Outline each blood parasite and name the species.
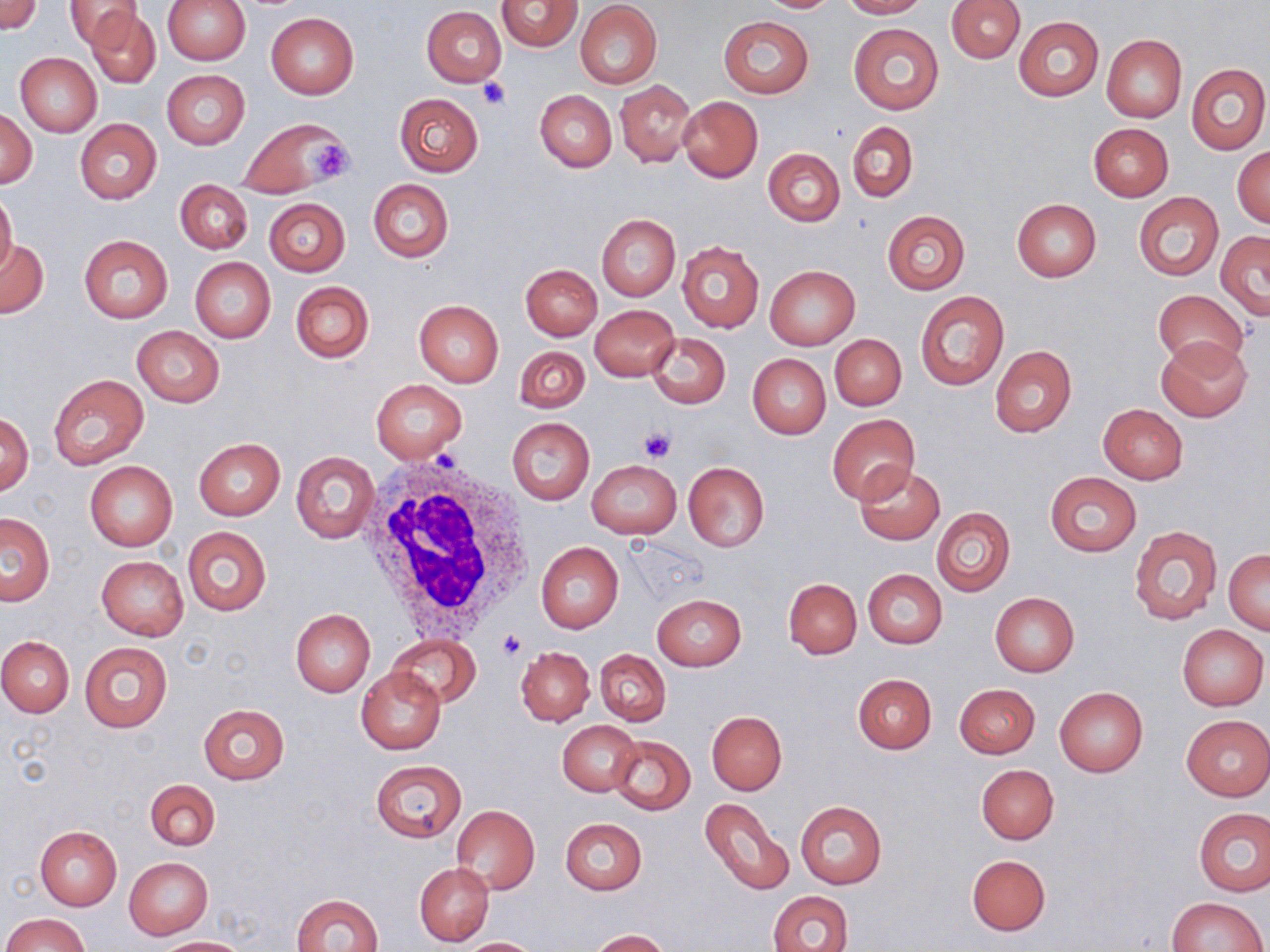

No blood parasites observed.

slide-level diagnosis = negative for blood parasites
field of view = single
image size = 1270×952 pixels
magnification = 1000x
modality = light microscopy
platelet locations = approximate bounding boxes as [x1, y1, x2, y2] in pixels: [477, 76, 511, 111], [307, 140, 355, 183], [639, 427, 674, 463], [498, 631, 525, 660]
preparation = thin blood film
uninfected red blood cell locations = approximate bounding boxes as [x1, y1, x2, y2] in pixels: [0, 0, 41, 35], [64, 0, 143, 50], [163, 0, 250, 64], [496, 0, 582, 52], [755, 0, 842, 13], [839, 0, 926, 18], [946, 0, 1025, 63], [575, 2, 663, 89], [86, 6, 161, 87], [422, 6, 506, 87], [265, 12, 360, 98], [719, 16, 813, 99], [1013, 16, 1103, 100], [848, 21, 944, 115], [1102, 35, 1186, 121], [15, 52, 102, 137], [1186, 62, 1269, 154], [162, 70, 250, 149], [615, 81, 696, 167], [535, 90, 616, 171], [394, 93, 484, 176], [678, 96, 763, 182], [2, 106, 36, 189], [237, 118, 348, 198], [75, 120, 161, 203], [847, 122, 918, 202], [1088, 123, 1173, 200], [1232, 147, 1270, 228], [763, 148, 844, 226], [367, 178, 454, 263], [175, 181, 253, 253], [0, 190, 18, 279], [1133, 192, 1223, 281], [264, 198, 350, 276], [1012, 199, 1102, 282], [882, 211, 970, 293], [597, 214, 680, 300], [1215, 230, 1270, 320], [78, 235, 173, 323], [0, 240, 48, 319], [676, 240, 764, 333], [190, 257, 276, 343], [521, 264, 601, 341], [765, 265, 860, 350], [289, 281, 375, 363], [1153, 289, 1249, 369], [914, 291, 1009, 391], [414, 300, 504, 387], [589, 305, 679, 382], [132, 325, 224, 406], [645, 331, 731, 409], [830, 334, 906, 410], [1156, 335, 1253, 423], [990, 345, 1077, 437], [514, 346, 589, 413], [748, 354, 831, 439], [48, 374, 149, 471], [370, 378, 468, 463], [1098, 403, 1189, 483], [1, 413, 34, 495], [828, 414, 919, 504], [507, 417, 595, 504], [193, 438, 285, 519], [291, 451, 380, 544], [587, 460, 681, 538], [85, 462, 177, 551], [682, 462, 770, 551], [854, 465, 944, 545], [1044, 471, 1141, 557], [931, 506, 1015, 596], [1, 512, 54, 606], [1129, 524, 1222, 624], [182, 527, 271, 615], [536, 543, 623, 634], [1225, 549, 1269, 634], [96, 555, 189, 640], [862, 568, 947, 648], [784, 578, 861, 659], [990, 592, 1080, 676], [652, 594, 746, 671], [290, 609, 375, 697], [1177, 624, 1268, 710], [386, 634, 481, 707], [0, 635, 75, 717], [80, 641, 172, 733], [516, 647, 594, 726], [595, 650, 671, 726], [357, 666, 446, 754], [852, 673, 936, 754], [954, 683, 1040, 758], [1054, 686, 1148, 777], [197, 703, 289, 784], [706, 711, 787, 794], [1181, 715, 1270, 801], [558, 720, 642, 797], [609, 735, 695, 816], [370, 760, 467, 842], [976, 764, 1059, 843], [145, 779, 221, 850], [700, 798, 793, 896], [795, 801, 888, 889], [451, 805, 540, 896], [1193, 808, 1270, 896], [559, 817, 647, 895], [34, 825, 121, 910], [967, 854, 1051, 935], [124, 857, 213, 938], [415, 862, 494, 947], [769, 890, 853, 952], [292, 893, 383, 952], [1167, 896, 1266, 951], [4, 913, 88, 952], [589, 929, 670, 951], [155, 937, 248, 951], [459, 937, 547, 951]
stain = May-Grünwald-Giemsa
white blood cell locations = approximate bounding boxes as [x1, y1, x2, y2] in pixels: [361, 452, 536, 640]